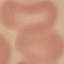
Summary:
  - Result: negative for malaria parasites
  - Stain: Giemsa
  - Capture: smartphone camera at the microscope eyepiece
  - Preparation: thin blood smear
  - Image type: cell patch, automatically extracted from a larger field of view and resized to 64 × 64 pixels